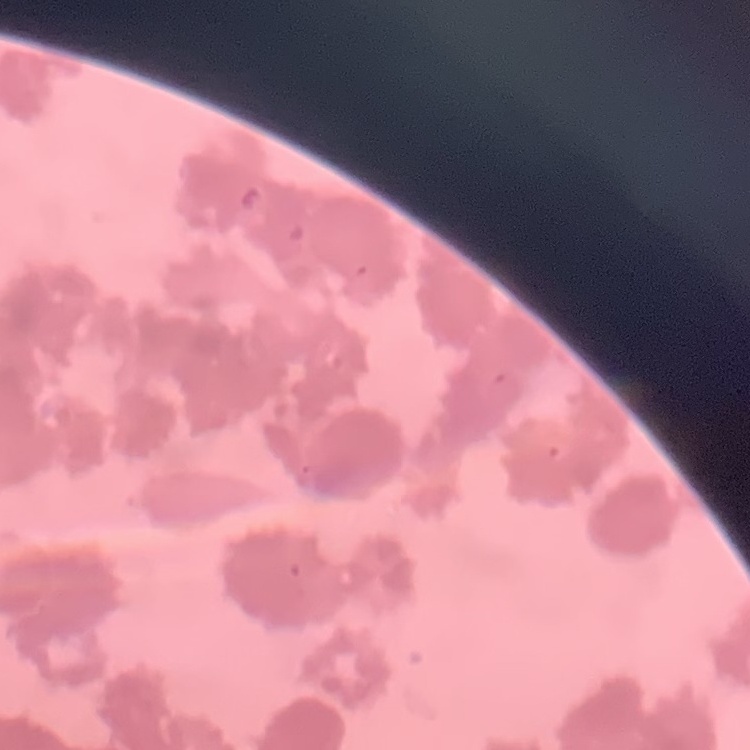

erythrocyte_morphology: rouleaux formation
preparation: thin blood film
image_type: square crop of a larger photomicrograph
stain: Field's or Giemsa